Assess the morphology of the erythrocytes.
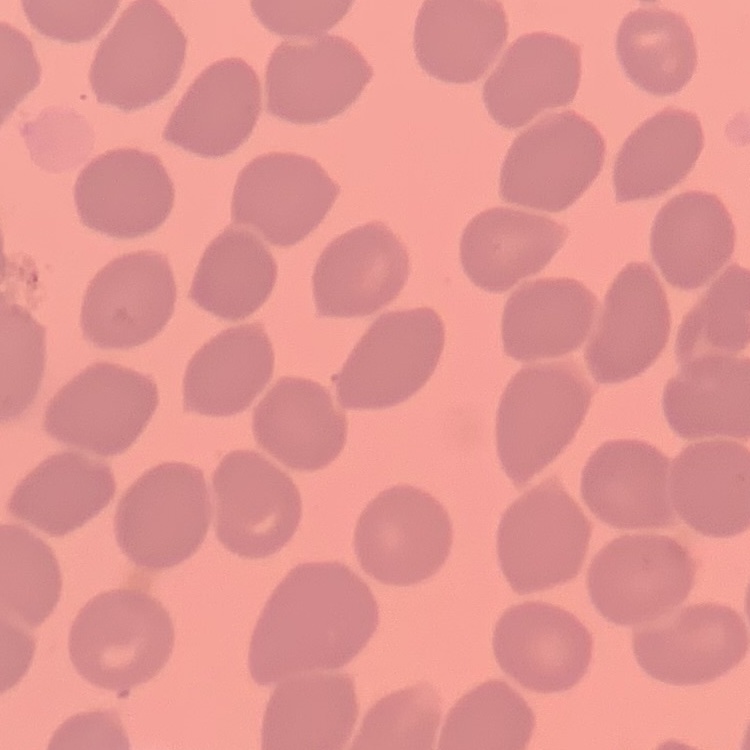

No rouleaux formation.

Thin blood film. One tile cut from a larger photomicrograph. Field's or Giemsa stain.